Report the malaria status of this cell.
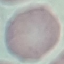

Uninfected.

capture = smartphone through the microscope eyepiece
stain = Giemsa
preparation = thin blood film
image type = automatically extracted cell patch, resized to 64 × 64 pixels